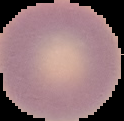
Summary:
  - Preparation: thin blood smear
  - Image type: cell region segmented out of the field of view; surrounding area masked to black
  - Malaria status: uninfected
  - Image size: 124×121 pixels